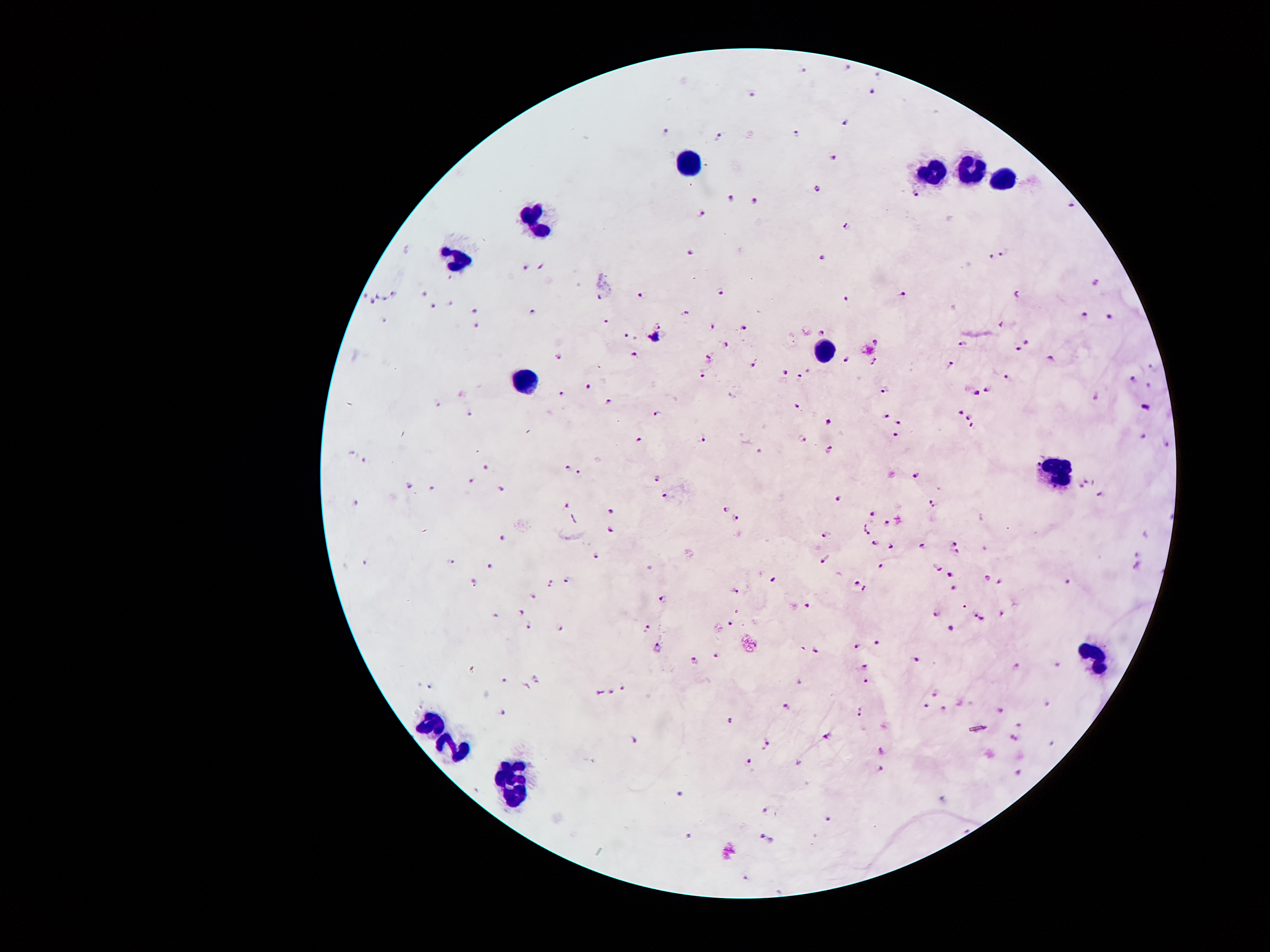 Thick blood film. Giemsa stain. 100x magnification. Image is 1270×952 pixels. One field from this slide. Patient malaria status: infected with Plasmodium falciparum. Photographed through the microscope eyepiece with a smartphone camera.